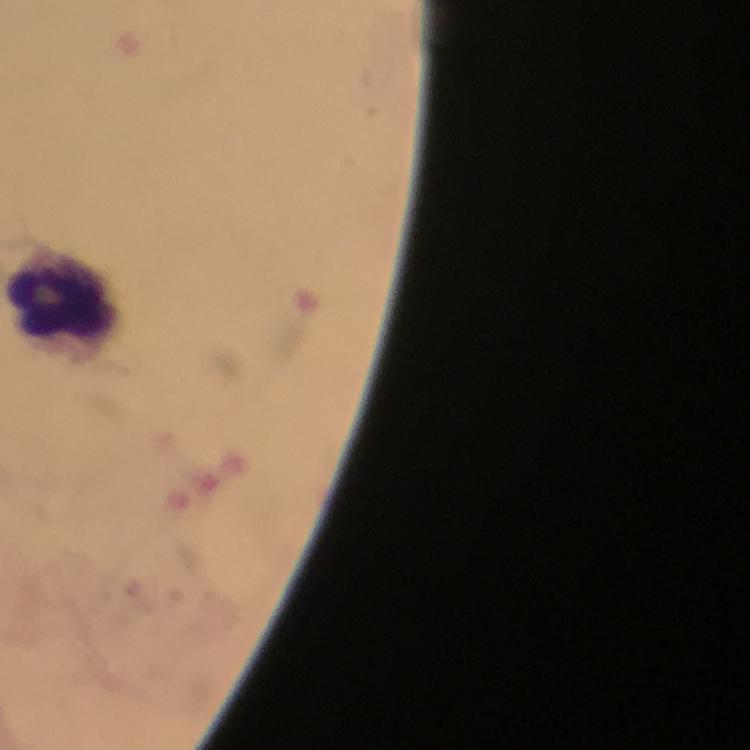
Approximate centers as (x, y) in pixels. Leukocyte locations: (71, 293). Giemsa-stained preparation. At 100x magnification. Immersion oil applied. Cropped region of a single field of view. Image is 750×750 pixels. Malaria parasites: none seen. From a diagnostic examination for malaria. Smartphone photograph taken through a microscope. Thick smear.